Report the malaria status of this cell.
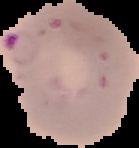
Parasitized.

Summary:
  - Image type: segmented cell region with the area outside set to black
  - Preparation: thin blood film
  - Image size: 139×148 pixels